Identify the parasite.
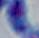

Toxoplasma gondii.

Captured at 1000x magnification. Photomicrograph.